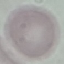

{
  "result": "no malaria parasites detected",
  "stain": "Giemsa",
  "capture": "smartphone through the microscope eyepiece",
  "image_type": "automatically extracted cell patch, resized to 64 × 64 pixels",
  "preparation": "thin blood film"
}